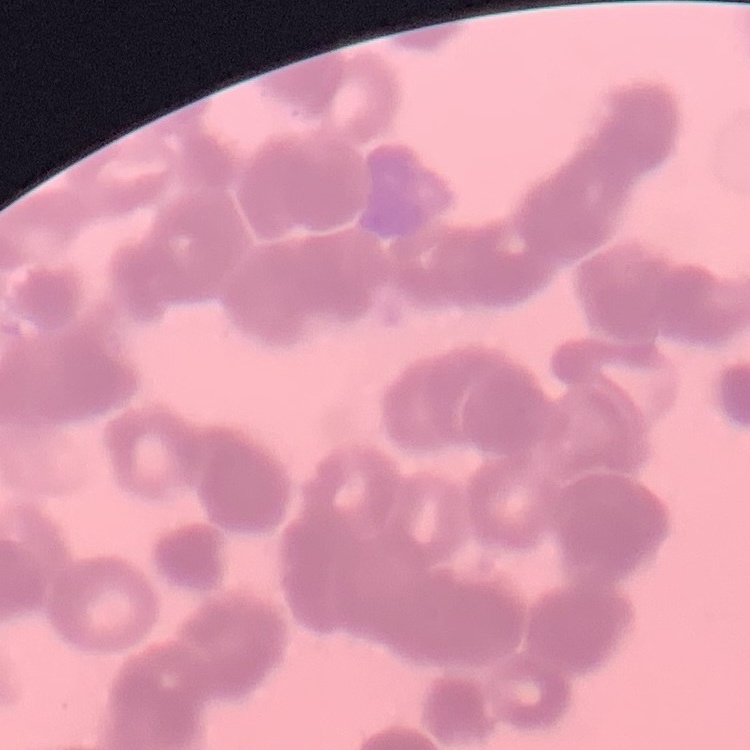

Summary:
  - Erythrocyte morphology: rouleaux formation
  - Image type: square crop of a larger photomicrograph
  - Preparation: thin blood film
  - Stain: Field's or Giemsa